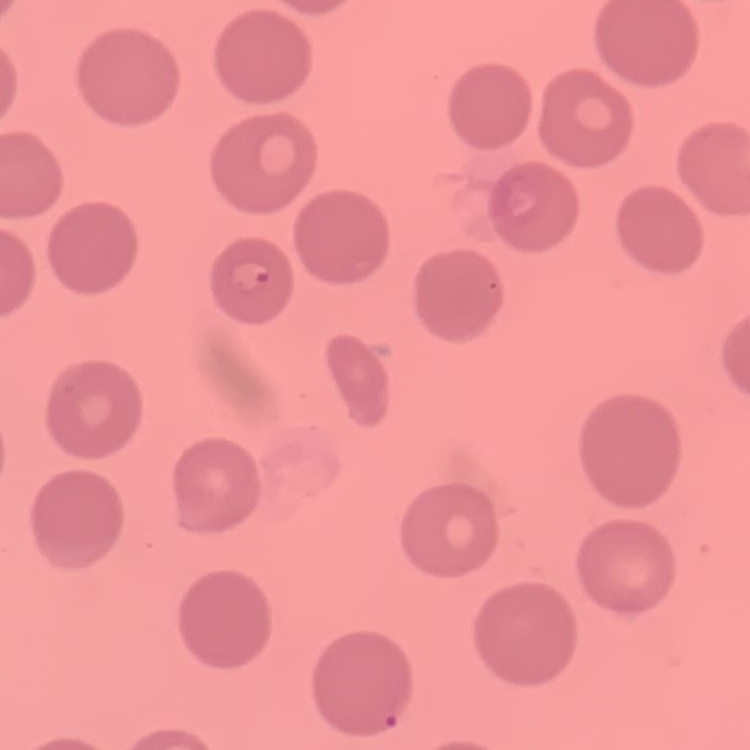

Summary:
  - Erythrocyte morphology: no rouleaux formation
  - Image type: square crop of a larger photomicrograph
  - Preparation: thin peripheral smear
  - Stain: Field's or Giemsa